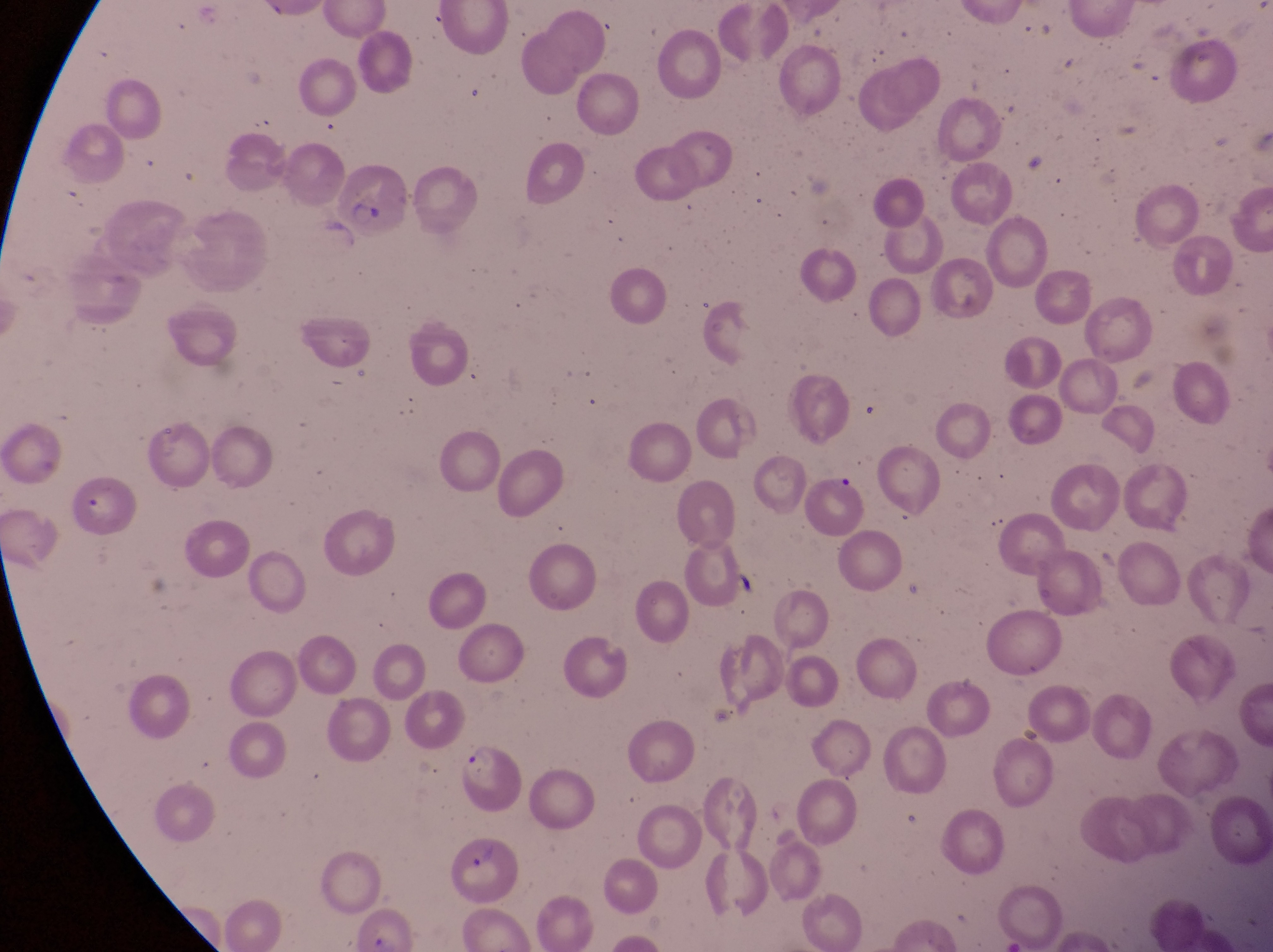

{
  "preparation": "thin blood film",
  "image_size": "1273×952 pixels",
  "magnification": "1000x",
  "country": "Uganda",
  "capture": "smartphone photograph through the eyepiece of an Olympus CX-23 microscope",
  "parasitised_red_blood_cell_locations": "approximate bounding boxes as [left, top, right, bottom] in pixels: [339, 167, 411, 237], [799, 467, 868, 537], [459, 741, 521, 816], [442, 832, 520, 907]",
  "field_of_view": "single"
}